State which cell type is depicted.
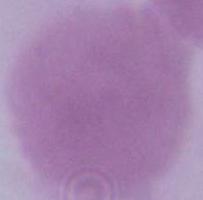

This is an erythrocyte.

Summary:
  - Modality: micrograph
  - Magnification: 1000x